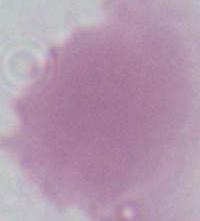

Summary:
  - Modality: micrograph
  - Identification: red blood cell
  - Magnification: 1000x